Give the position of every Plasmodium parasite visible.
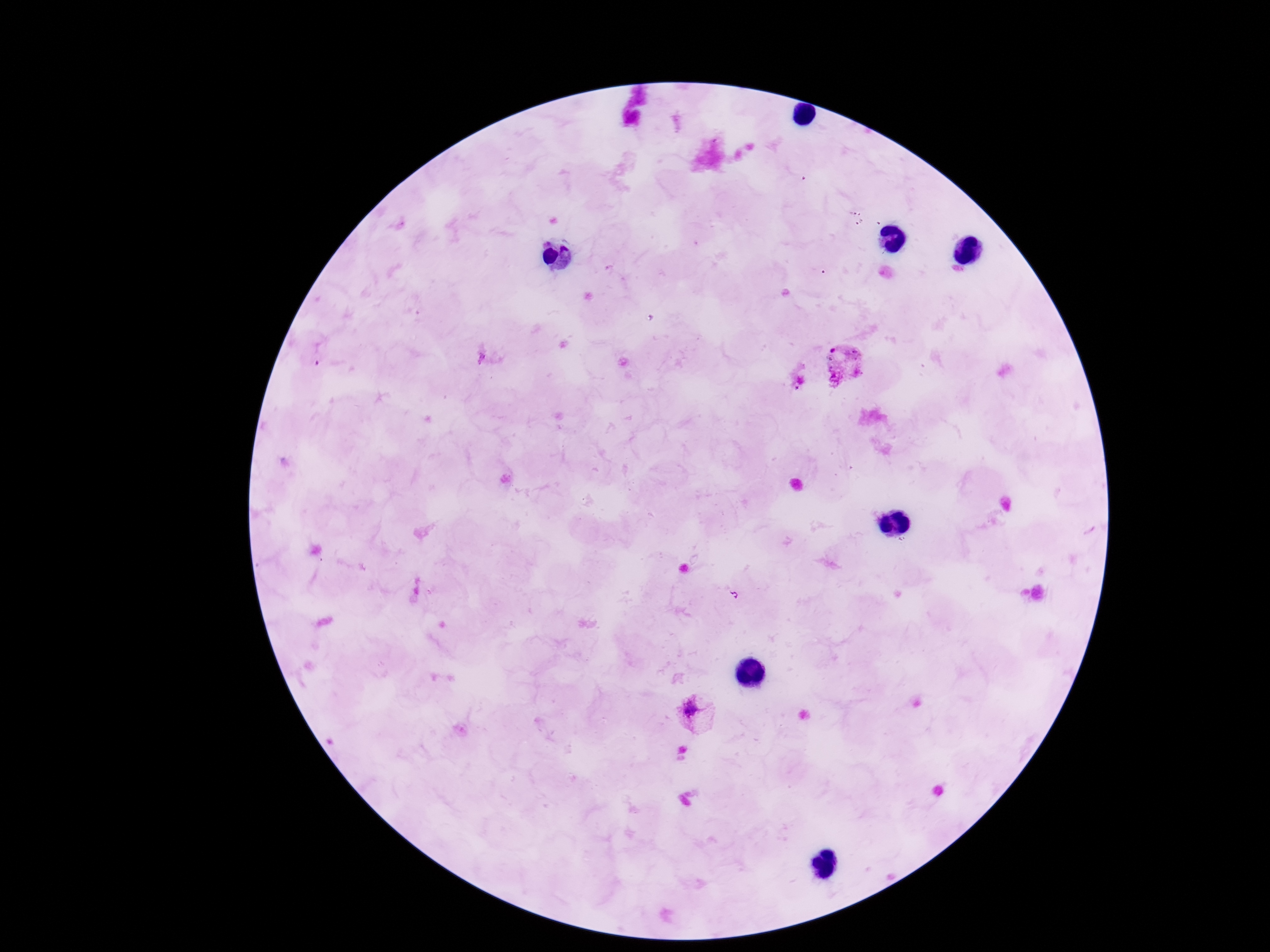
Approximate centers as [x, y] in pixels.
Plasmodium parasites: [845, 361], [696, 712].

capture: smartphone camera through the microscope eyepiece
preparation: thick peripheral-blood smear
image_size: 1270×952 pixels
stain: Giemsa
patient_malaria_status: positive
field_of_view: one from this slide
magnification: 100x